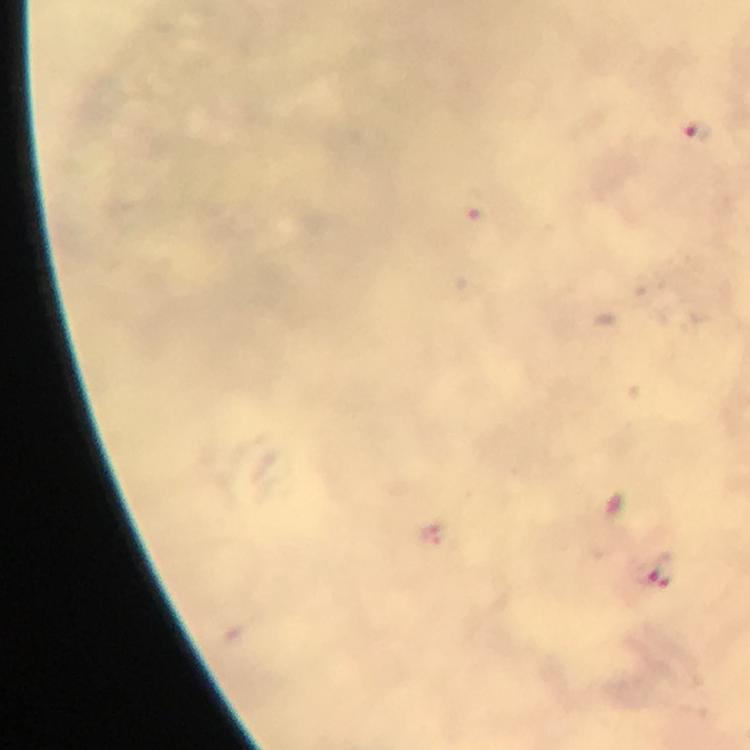 Approximate object centers, in pixels from the top-left corner. Malaria parasite locations: (x=696, y=129), (x=435, y=536), (x=658, y=570). A crop from one field of view. 100x magnification. From a malaria diagnostic workup. Immersion oil applied. Smartphone photograph taken through a microscope. Image is 750×750 pixels. Giemsa stain. Thick blood film.